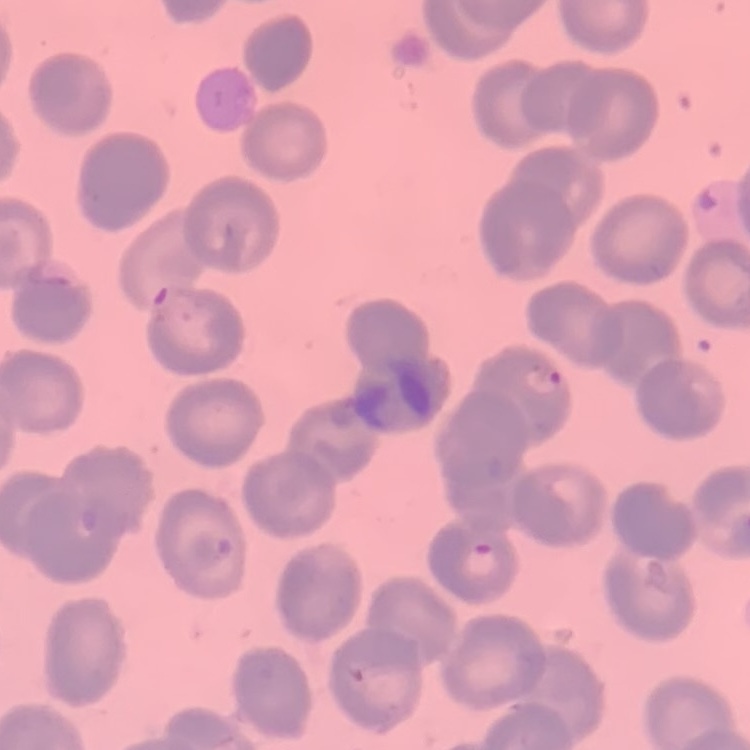

Summary:
  - Erythrocyte morphology: no rouleaux formation
  - Stain: Field's or Giemsa
  - Preparation: thin blood film
  - Image type: square crop of a larger photomicrograph